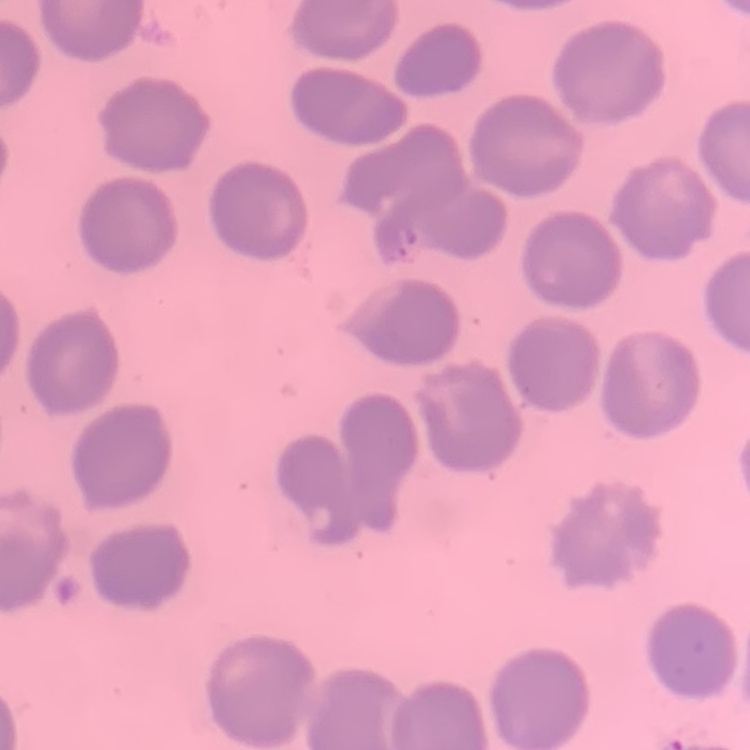
Summary:
  - Red blood cell morphology: no rouleaux formation
  - Image type: one tile cut from a larger photomicrograph
  - Stain: Field's or Giemsa
  - Preparation: thin blood film